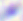

magnification = 400x
identification = Toxoplasma gondii
modality = micrograph